Locate and identify every blood parasite.
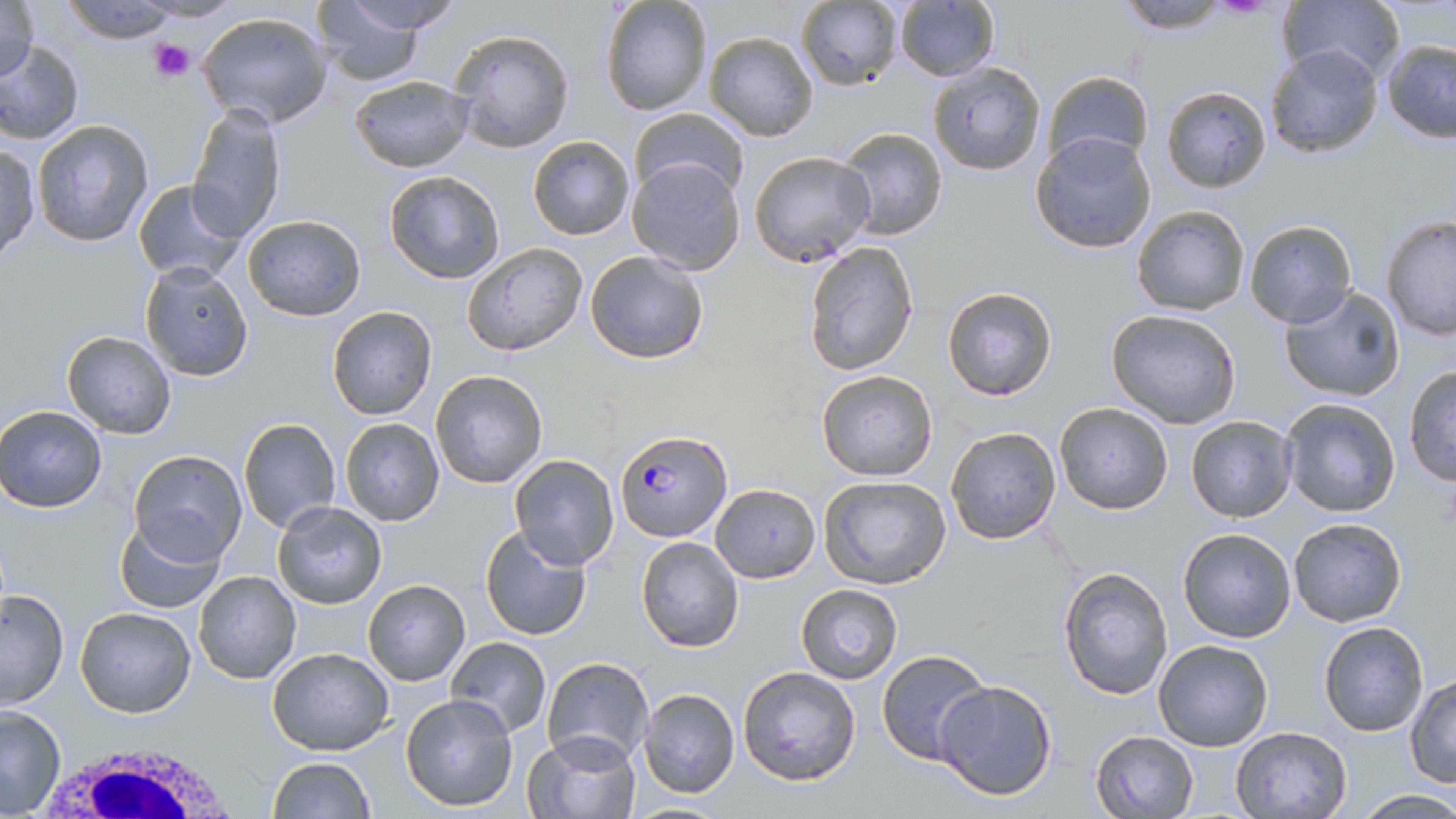
Approximate bounding boxes as [x1, y1, x2, y2] in pixels.
Plasmodium falciparum-infected red blood cells: [617, 428, 731, 543].
No Plasmodium ovale, Plasmodium malariae, Plasmodium vivax, Babesia divergens, or Trypanosoma brucei observed.

White blood cell locations: [23, 728, 253, 819]. Platelet locations: [148, 38, 195, 83]. Uninfected red blood cell locations: [0, 0, 41, 86], [59, 0, 186, 44], [334, 0, 464, 34], [598, 0, 714, 116], [1111, 0, 1240, 34], [1275, 0, 1407, 85], [795, 1, 904, 89], [893, 1, 1000, 83], [315, 6, 438, 83], [196, 12, 331, 128], [448, 29, 574, 153], [702, 30, 818, 141], [0, 39, 83, 144], [1380, 39, 1456, 142], [1262, 45, 1383, 158], [927, 60, 1048, 177], [1042, 71, 1153, 168], [348, 74, 474, 172], [1161, 86, 1270, 192], [186, 103, 287, 241], [627, 108, 749, 202], [31, 120, 155, 247], [833, 125, 948, 241], [1031, 130, 1157, 254], [526, 135, 634, 240], [0, 142, 40, 261], [748, 150, 875, 266], [626, 156, 746, 275], [383, 171, 507, 283], [130, 178, 249, 286], [1132, 205, 1250, 315], [242, 214, 366, 321], [1380, 214, 1456, 339], [1243, 219, 1359, 330], [803, 241, 923, 376], [462, 242, 589, 357], [584, 249, 710, 365], [140, 262, 254, 382], [941, 285, 1060, 401], [1277, 285, 1407, 403], [326, 306, 438, 420], [1104, 308, 1243, 428], [61, 329, 177, 440], [1403, 365, 1455, 485], [815, 368, 939, 481], [430, 369, 548, 489], [1279, 397, 1402, 518], [1053, 402, 1175, 515], [1, 405, 107, 513], [1186, 415, 1297, 522], [238, 417, 342, 535], [339, 417, 445, 526], [945, 425, 1062, 544], [128, 449, 248, 565], [508, 455, 621, 571], [819, 474, 952, 589], [709, 482, 821, 584], [274, 501, 388, 610], [112, 516, 227, 613], [1287, 516, 1407, 627], [479, 524, 592, 642], [1175, 528, 1297, 643], [635, 536, 744, 652], [1058, 566, 1175, 700], [192, 569, 302, 684], [363, 579, 470, 687], [796, 583, 903, 684], [0, 590, 70, 708], [74, 605, 196, 717], [1318, 621, 1429, 736], [445, 636, 550, 738], [1152, 639, 1273, 752], [267, 646, 394, 755], [876, 649, 995, 765], [540, 656, 653, 769], [736, 666, 862, 787], [1404, 673, 1456, 788], [934, 680, 1056, 801], [637, 687, 741, 799], [401, 693, 519, 813], [0, 705, 66, 816], [1229, 727, 1352, 818], [1091, 729, 1199, 818], [525, 730, 642, 819], [267, 757, 377, 818], [1350, 788, 1456, 818]. Slide-level diagnosis: Plasmodium falciparum. One field of a larger specimen. Optical microscopy. Thin blood smear. May-Grünwald-Giemsa-stained preparation. Image is 1456×819 pixels. Captured at 1000x magnification.